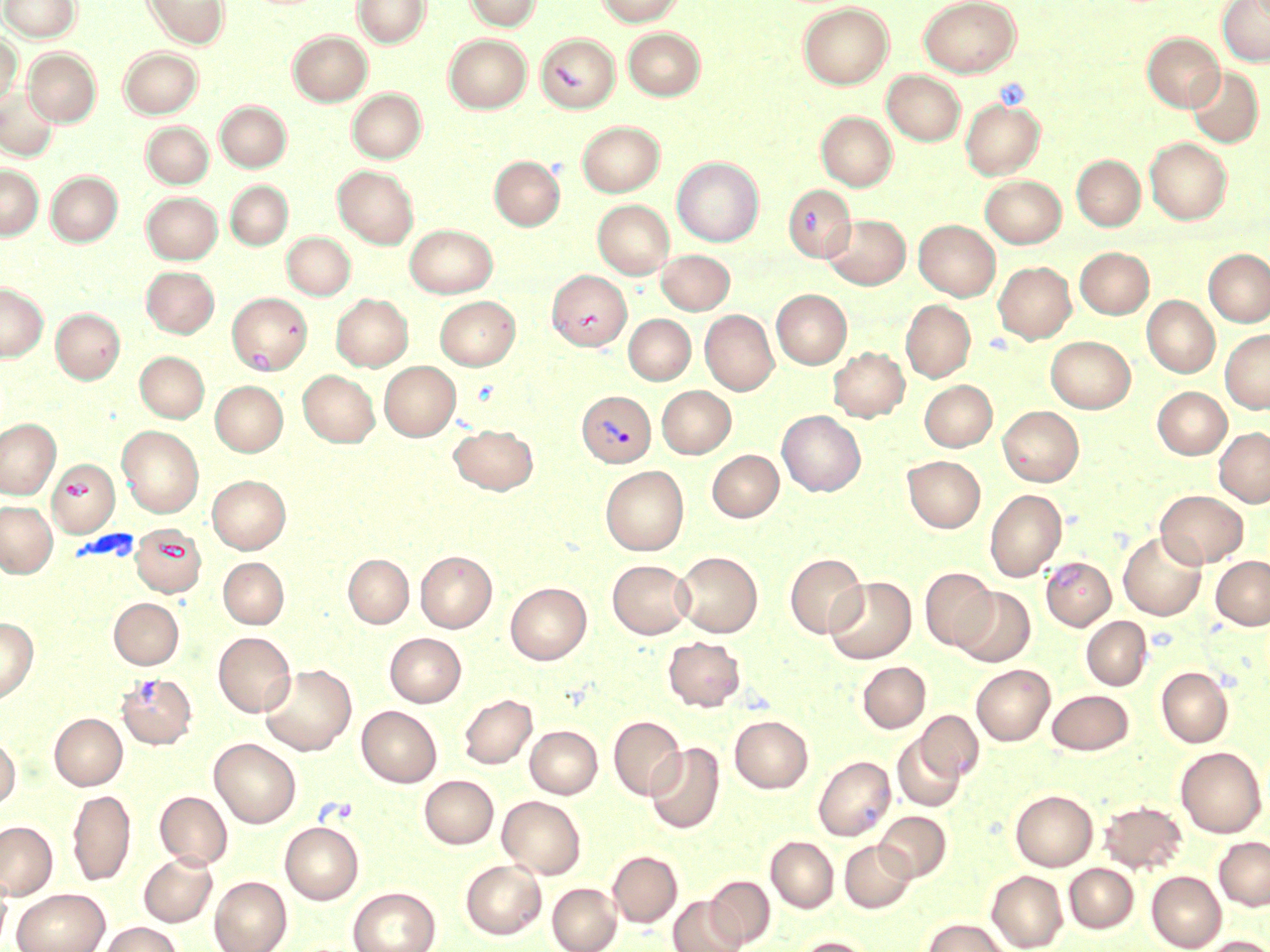

Approximate bounding boxes as (x1,y1)-(x2,y2) corner pairs in pixels. Platelet locations: (317,796)-(360,824). Plasmodium vivax-infected red blood cell locations: (577,391)-(655,467). Uninfected red blood cell locations: (0,0)-(80,41), (144,0)-(229,48), (353,0)-(430,48), (464,0)-(540,31), (597,0)-(684,26), (918,0)-(1021,77), (1217,1)-(1270,66), (798,3)-(893,89), (623,28)-(705,100), (289,31)-(372,105), (1142,32)-(1224,111), (536,33)-(619,113), (0,34)-(22,108), (444,35)-(531,112), (24,48)-(101,126), (119,48)-(203,118), (1186,66)-(1263,148), (882,71)-(966,145), (1,87)-(59,160), (347,89)-(426,162), (960,97)-(1045,179), (215,101)-(291,171), (816,112)-(896,190), (141,121)-(213,188), (577,121)-(665,196), (1145,138)-(1231,224), (1071,155)-(1145,231), (490,156)-(564,230), (673,157)-(764,246), (0,166)-(43,239), (333,166)-(418,248), (46,171)-(122,245), (980,176)-(1065,247), (226,181)-(292,249), (784,185)-(855,261), (142,192)-(222,263), (593,200)-(674,278), (823,214)-(910,289), (914,220)-(1000,300), (405,225)-(497,297), (282,232)-(355,299), (1075,247)-(1154,318), (1204,249)-(1270,327), (656,250)-(734,314), (994,261)-(1076,343), (142,266)-(219,337), (547,271)-(631,349), (0,283)-(48,361), (772,290)-(851,368), (331,294)-(413,371), (229,295)-(312,376), (1142,295)-(1220,378), (435,296)-(520,369), (901,300)-(975,382), (51,308)-(125,384), (700,309)-(778,395), (623,314)-(695,384), (1220,329)-(1270,414), (1046,336)-(1135,413), (828,347)-(909,422), (135,351)-(208,422), (380,361)-(460,440), (299,370)-(379,446), (920,380)-(997,451), (211,381)-(287,455), (657,386)-(735,458), (1152,386)-(1231,459), (997,406)-(1084,486), (777,411)-(865,496), (0,419)-(60,498), (449,424)-(538,494), (118,426)-(204,517), (1214,427)-(1270,507), (707,450)-(783,521), (902,455)-(985,532), (47,459)-(119,536), (600,466)-(688,555), (207,475)-(290,553), (985,488)-(1067,581), (1155,490)-(1248,568), (0,501)-(57,577), (130,524)-(206,597), (1118,531)-(1207,620), (415,551)-(497,632), (673,551)-(762,637), (784,553)-(867,638), (343,554)-(413,628), (1211,556)-(1270,629), (218,557)-(289,629), (1041,558)-(1115,630), (608,560)-(693,639), (920,567)-(997,652), (824,576)-(916,663), (505,582)-(591,664), (953,587)-(1035,667), (109,598)-(183,669), (1082,616)-(1151,690), (0,618)-(38,703), (214,632)-(296,717), (384,633)-(465,707), (663,636)-(746,711), (858,661)-(930,732), (260,664)-(357,755), (972,664)-(1055,745), (1156,666)-(1233,747), (117,673)-(196,749), (1047,689)-(1133,754), (459,693)-(537,769), (357,706)-(442,786), (916,710)-(983,782), (50,713)-(127,790), (608,715)-(686,800), (729,715)-(813,792), (525,725)-(602,798), (0,735)-(20,809), (893,735)-(965,811), (210,738)-(300,827), (645,742)-(724,834), (1176,746)-(1266,837), (814,755)-(895,841), (419,775)-(498,848), (67,789)-(136,886), (1011,790)-(1097,870), (155,791)-(232,869), (497,796)-(586,878), (1099,800)-(1187,874), (875,811)-(951,881), (0,821)-(57,900), (280,821)-(364,904), (766,836)-(839,913), (1214,836)-(1270,910), (840,840)-(916,912), (607,851)-(682,927), (139,853)-(217,927), (460,859)-(546,939), (1064,863)-(1138,933), (987,870)-(1067,951), (1147,871)-(1226,951), (0,872)-(12,949), (706,875)-(775,948), (209,876)-(291,952), (547,882)-(622,952), (347,886)-(440,952), (12,888)-(109,952), (668,896)-(746,952), (923,918)-(1009,952), (99,922)-(182,952), (795,936)-(874,952), (1198,936)-(1270,952). Slide-level diagnosis: Plasmodium vivax. May-Grünwald-Giemsa stain. Image is 1270×952 pixels. Thin blood smear. Optical microscopy. Single field of view. 1000x magnification.